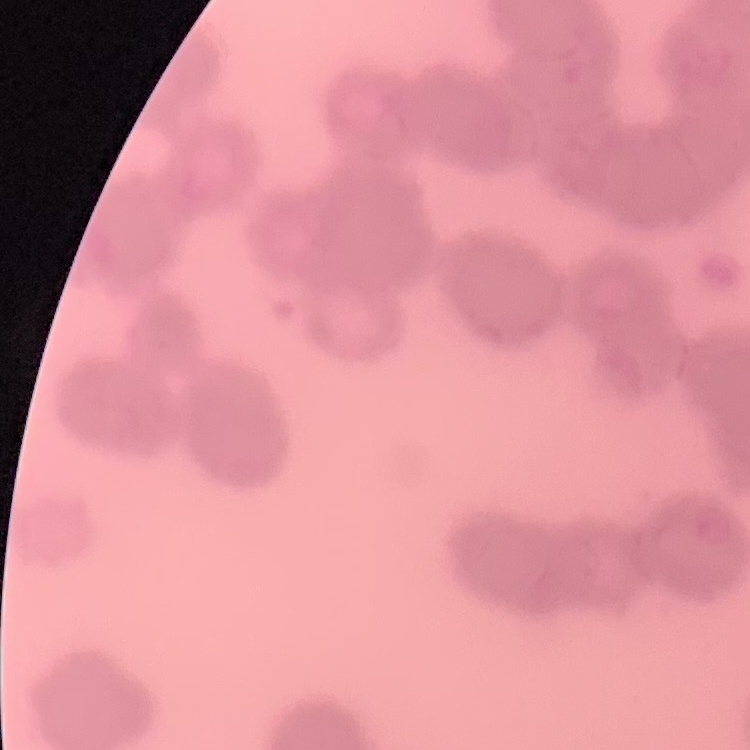

{
  "erythrocyte_morphology": "rouleaux formation",
  "preparation": "thin blood film",
  "image_type": "square crop of a larger photomicrograph",
  "stain": "Field's or Giemsa"
}